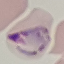
Summary:
  - Malaria status: uninfected
  - Capture: smartphone through the microscope eyepiece
  - Preparation: thin blood smear
  - Stain: Giemsa
  - Image type: cell patch, automatically extracted from a larger field of view and resized to 64 × 64 pixels